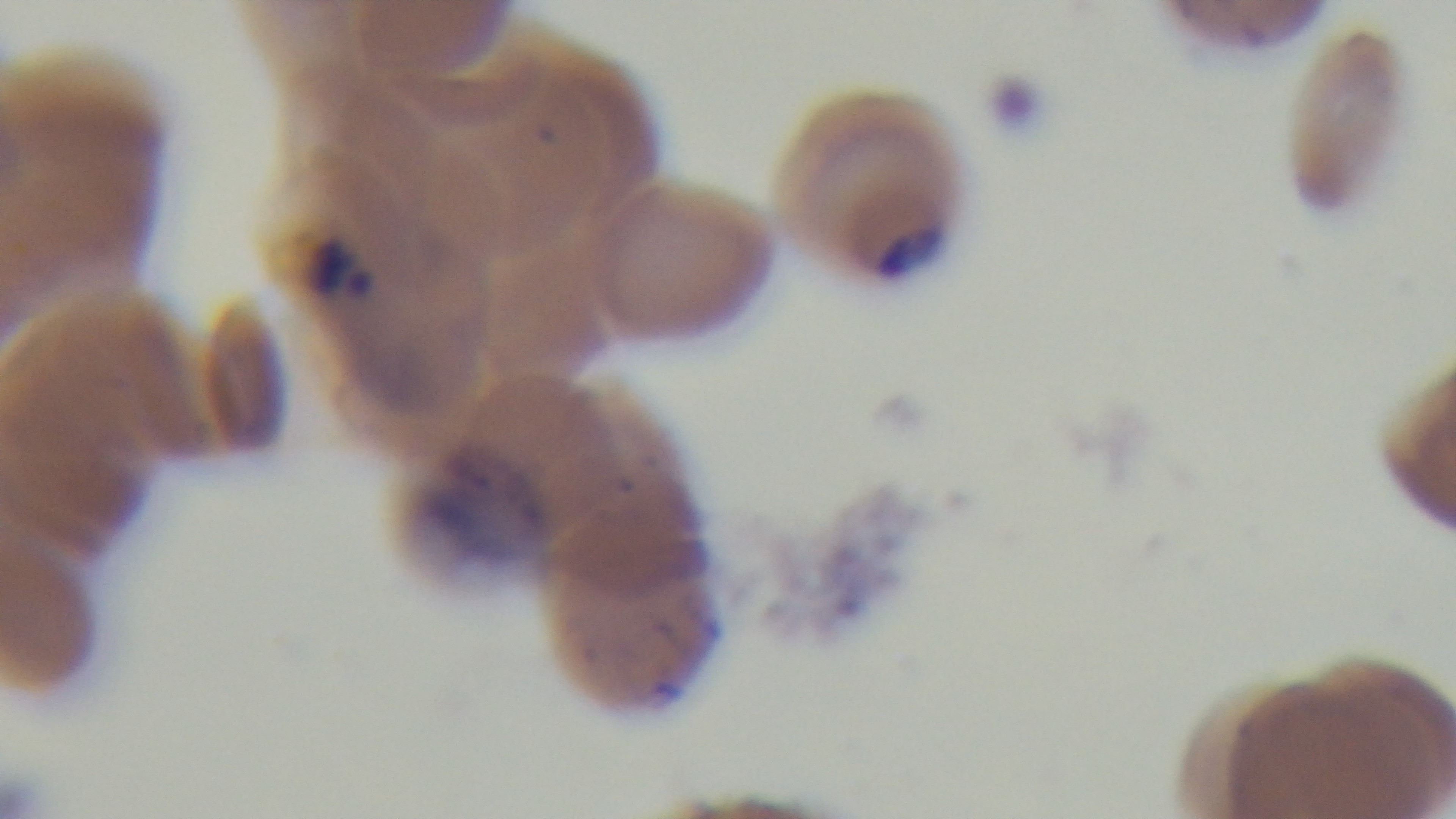 One field from the slide. Preparation: thin. Giemsa-stained. Photomicrograph. 100x oil-immersion objective. Captured with a mounted 4K digital camera. Malaria status: positive.